Report the malaria status of this cell.
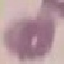

Uninfected.

Thin blood smear. Automatically extracted cell patch, resized to 64 × 64 pixels. Acquired by smartphone through the microscope eyepiece. Giemsa-stained preparation.